Locate and identify every blood parasite.
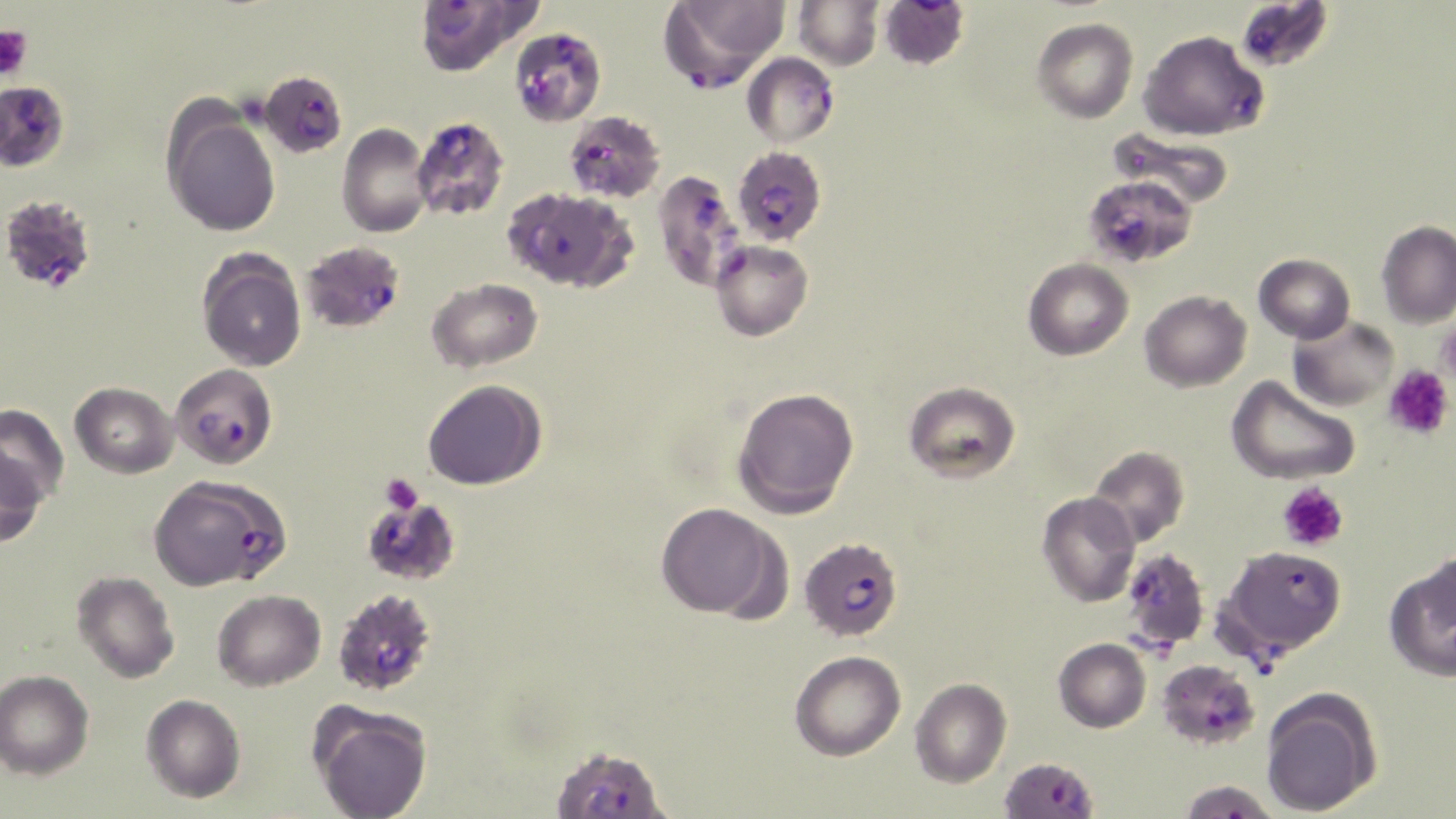
Approximate bounding boxes as (x1, y1, x2, y2) in pixels.
Plasmodium falciparum-infected red blood cells: (413, 0, 536, 77), (656, 0, 789, 91), (878, 0, 970, 73), (1235, 1, 1335, 73), (517, 29, 603, 123), (1137, 29, 1267, 141), (742, 52, 840, 148), (258, 70, 348, 158), (0, 80, 69, 170), (564, 110, 666, 203), (411, 116, 510, 220), (733, 146, 827, 246), (652, 169, 748, 292), (1084, 173, 1198, 268), (502, 186, 636, 292), (0, 193, 97, 294), (300, 241, 405, 334), (169, 363, 278, 469), (159, 479, 303, 593), (360, 491, 462, 586), (798, 537, 903, 641), (1219, 545, 1347, 674), (1120, 548, 1210, 652), (332, 587, 439, 697), (1156, 659, 1260, 751), (550, 744, 670, 819), (998, 757, 1099, 819), (1177, 779, 1280, 818).
No Plasmodium ovale, Plasmodium malariae, Plasmodium vivax, Babesia divergens, or Trypanosoma brucei observed.

Summary:
  - Platelet locations: (0, 24, 33, 82), (1383, 365, 1454, 441), (381, 473, 423, 513), (1277, 481, 1349, 551)
  - Uninfected red blood cell locations: (793, 0, 883, 71), (1032, 17, 1139, 123), (161, 105, 281, 238), (337, 123, 432, 238), (1107, 125, 1236, 210), (1376, 220, 1456, 328), (710, 239, 814, 342), (197, 248, 307, 372), (1253, 253, 1355, 343), (1023, 257, 1133, 360), (427, 277, 543, 372), (1139, 290, 1252, 392), (1288, 315, 1398, 412), (1226, 375, 1360, 485), (422, 379, 546, 490), (903, 380, 1020, 483), (70, 382, 178, 479), (732, 387, 860, 517), (0, 404, 69, 506), (1087, 445, 1190, 547), (0, 448, 46, 551), (1036, 491, 1141, 607), (655, 502, 784, 619), (1382, 555, 1456, 682), (71, 571, 179, 683), (212, 589, 326, 691), (1053, 637, 1151, 732), (789, 650, 906, 761), (0, 669, 94, 780), (910, 677, 1011, 787), (1260, 687, 1382, 817), (141, 694, 246, 803), (309, 703, 433, 819)
  - Slide-level diagnosis: Plasmodium falciparum
  - Image size: 1456×819 pixels
  - Field of view: one of a larger specimen
  - Magnification: 1000x
  - Stain: May-Grünwald-Giemsa
  - Modality: light microscopy
  - Preparation: thin blood smear